Locate every Plasmodium ovale-infected red blood cell.
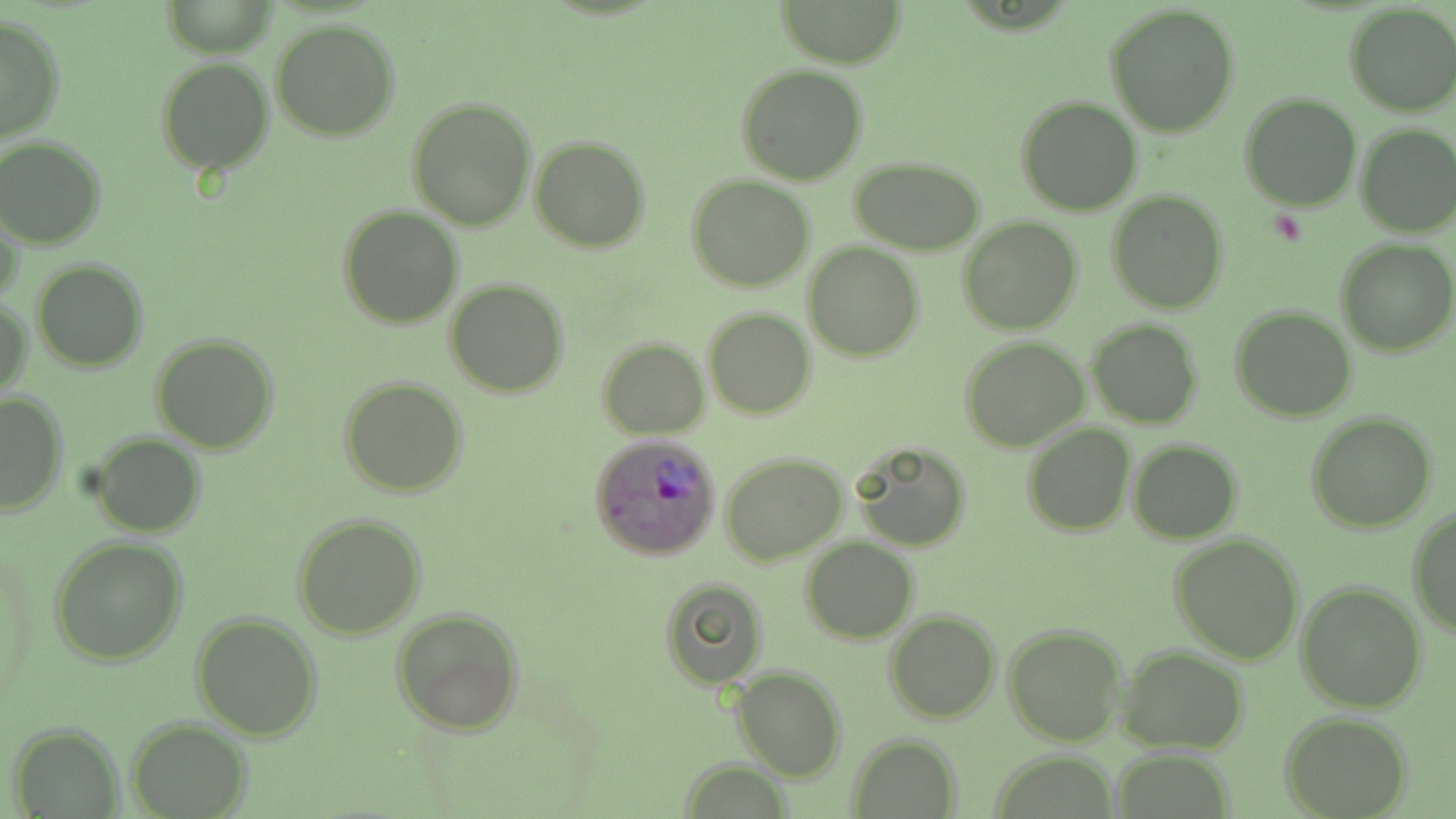

Approximate bounding boxes as (x1, y1, x2, y2) in pixels.
Plasmodium ovale-infected red blood cells: (591, 433, 722, 559).

Summary:
  - Uninfected red blood cell locations: (775, 0, 910, 67), (1343, 4, 1456, 117), (1106, 5, 1240, 136), (0, 16, 65, 142), (270, 17, 402, 141), (155, 57, 273, 174), (735, 65, 867, 186), (1240, 92, 1362, 211), (1015, 96, 1142, 217), (406, 98, 535, 231), (1355, 125, 1456, 237), (0, 136, 106, 249), (531, 136, 651, 254), (850, 159, 987, 254), (687, 174, 815, 292), (1108, 190, 1228, 312), (0, 202, 26, 311), (338, 206, 462, 330), (958, 218, 1082, 335), (1335, 238, 1456, 357), (803, 243, 923, 363), (31, 259, 150, 371), (445, 279, 569, 398), (1, 296, 32, 402), (1231, 306, 1357, 423), (703, 307, 816, 420), (1085, 319, 1203, 428), (150, 334, 279, 454), (597, 336, 709, 440), (960, 337, 1090, 451), (339, 378, 467, 497), (0, 391, 68, 517), (1305, 412, 1437, 532), (1023, 424, 1135, 536), (90, 433, 205, 538), (849, 440, 971, 551), (1128, 440, 1243, 544), (721, 454, 847, 566), (1407, 504, 1456, 638), (292, 514, 426, 640), (1170, 534, 1304, 665), (49, 536, 188, 665), (800, 537, 919, 644), (657, 576, 770, 688), (1295, 581, 1428, 712), (391, 607, 524, 735), (884, 610, 1000, 724), (191, 613, 322, 741), (1003, 623, 1128, 746), (1117, 645, 1250, 754), (732, 666, 845, 782), (1280, 713, 1412, 818), (127, 718, 251, 817), (10, 723, 121, 816), (846, 734, 962, 817), (1112, 750, 1238, 818), (676, 761, 796, 817)
  - Slide-level diagnosis: Plasmodium ovale
  - Stain: May-Grünwald-Giemsa
  - Magnification: 1000x
  - Preparation: thin blood smear
  - Image size: 1456×819 pixels
  - Field of view: one of a larger specimen
  - Modality: optical microscopy